Classify this cell by malaria status.
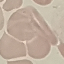

Uninfected.

preparation: thin blood smear
stain: Giemsa
image_type: automatically extracted cell patch, resized to 64 × 64 pixels
capture: smartphone through the microscope eyepiece